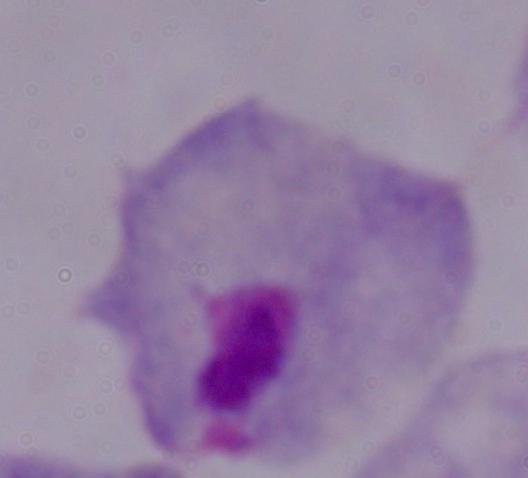 A trichomonad is seen. Photomicrograph. Captured at 1000x magnification.